Name the parasite shown.
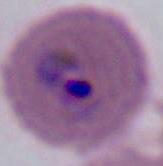

Plasmodium.

modality = micrograph
magnification = 400x or 1000x